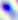
Toxoplasma gondii is seen. Captured at 400x magnification. Micrograph.